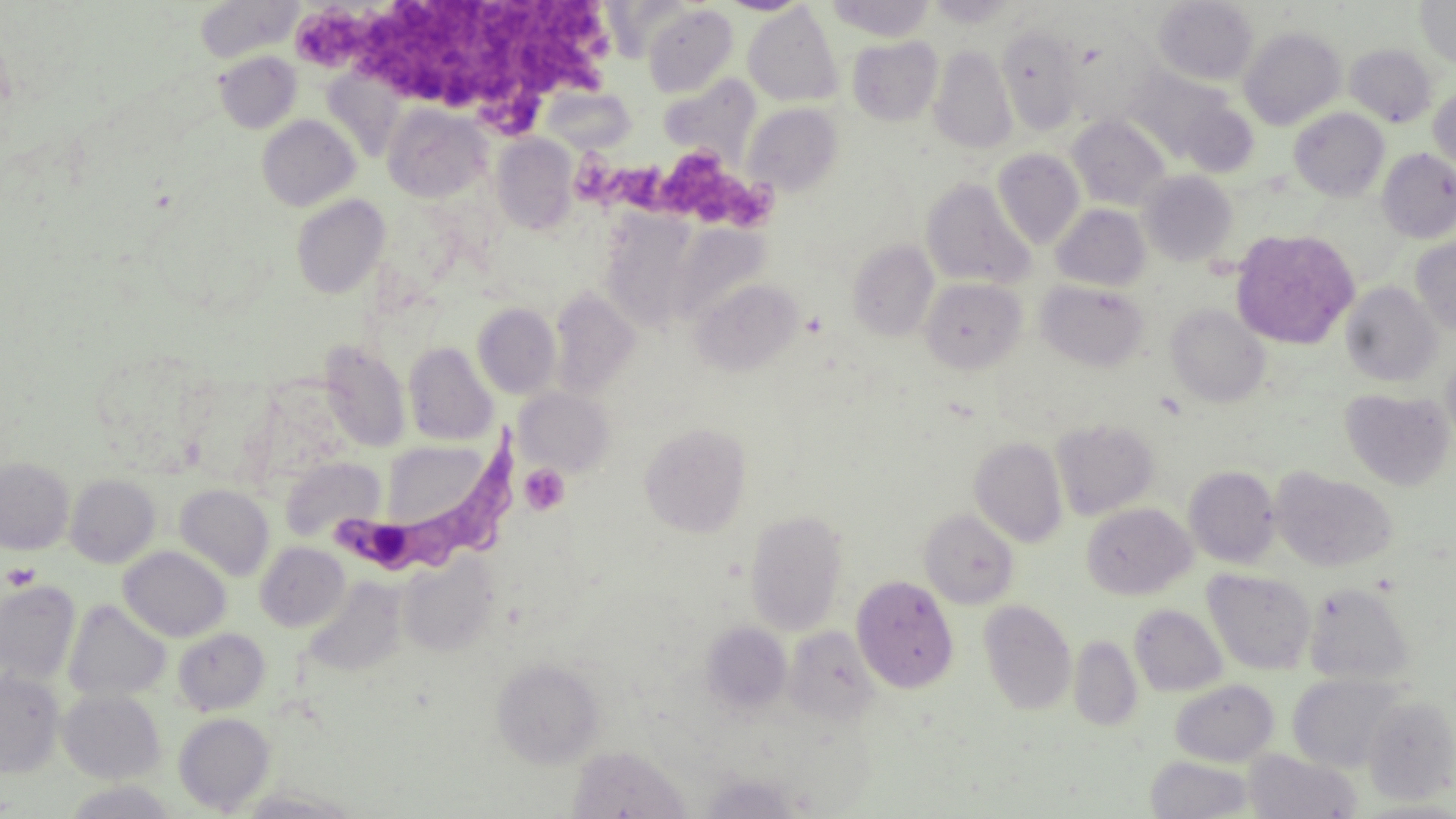

slide-level diagnosis = Trypanosoma brucei
field of view = one of a larger specimen
image size = 1456×819 pixels
magnification = 1000x
platelet locations = approximate bounding boxes as (x1,y1)-(x2,y2) corner pairs in pixels: (303,0)-(611,127), (572,143)-(776,223), (519,464)-(570,515), (3,562)-(41,590)
uninfected red blood cell locations = approximate bounding boxes as (x1,y1)-(x2,y2) corner pairs in pixels: (719,0)-(811,15), (828,0)-(934,41), (926,0)-(1021,27), (1153,0)-(1258,86), (1415,0)-(1456,68), (197,1)-(300,61), (643,4)-(738,97), (744,4)-(843,107), (997,25)-(1083,134), (1239,26)-(1346,130), (1063,33)-(1157,127), (848,36)-(943,125), (1344,44)-(1438,127), (930,45)-(1016,154), (215,51)-(301,133), (1122,64)-(1246,167), (659,75)-(759,163), (1429,85)-(1456,174), (541,86)-(636,154), (743,103)-(843,197), (383,104)-(491,202), (1289,108)-(1389,201), (257,114)-(360,211), (1067,115)-(1170,211), (492,135)-(578,234), (992,148)-(1085,249), (1377,148)-(1456,244), (1140,171)-(1237,266), (920,177)-(1035,290), (291,194)-(390,299), (1051,204)-(1150,291), (1232,228)-(1360,350), (1411,237)-(1456,337), (847,240)-(939,341), (690,277)-(803,376), (920,277)-(1026,374), (1036,280)-(1150,371), (1341,282)-(1443,387), (548,288)-(639,398), (472,302)-(561,399), (1166,304)-(1270,407), (320,341)-(411,452), (403,342)-(498,445), (1442,348)-(1456,450), (515,388)-(614,475), (1340,388)-(1453,491), (1051,418)-(1159,521), (639,421)-(752,538), (969,436)-(1068,547), (379,440)-(488,531), (0,456)-(74,554), (280,457)-(385,543), (1184,466)-(1280,568), (1272,468)-(1398,573), (65,474)-(160,568), (175,483)-(275,581), (1082,502)-(1195,600), (745,509)-(849,635), (919,509)-(1019,609), (255,542)-(350,631), (119,546)-(231,642), (398,555)-(499,657), (1203,568)-(1317,674), (851,575)-(959,693), (302,579)-(405,679), (1,581)-(81,684), (1304,581)-(1416,684), (63,599)-(172,702), (979,599)-(1077,716), (1130,604)-(1227,696), (701,622)-(792,715), (784,626)-(880,725), (174,628)-(270,715), (1069,635)-(1143,732), (491,657)-(605,768), (0,670)-(65,777), (1288,673)-(1407,772), (1170,679)-(1279,766), (58,688)-(166,783), (1362,694)-(1456,804), (173,712)-(275,813), (566,744)-(693,818), (1244,750)-(1362,818), (1145,756)-(1256,818), (700,772)-(804,818), (1357,798)-(1456,818)
Trypanosoma brucei locations = approximate bounding boxes as (x1,y1)-(x2,y2) corner pairs in pixels: (338,423)-(525,573)
modality = optical microscopy
stain = May-Grünwald-Giemsa
preparation = thin blood smear